Locate every leukocyte (white blood cell).
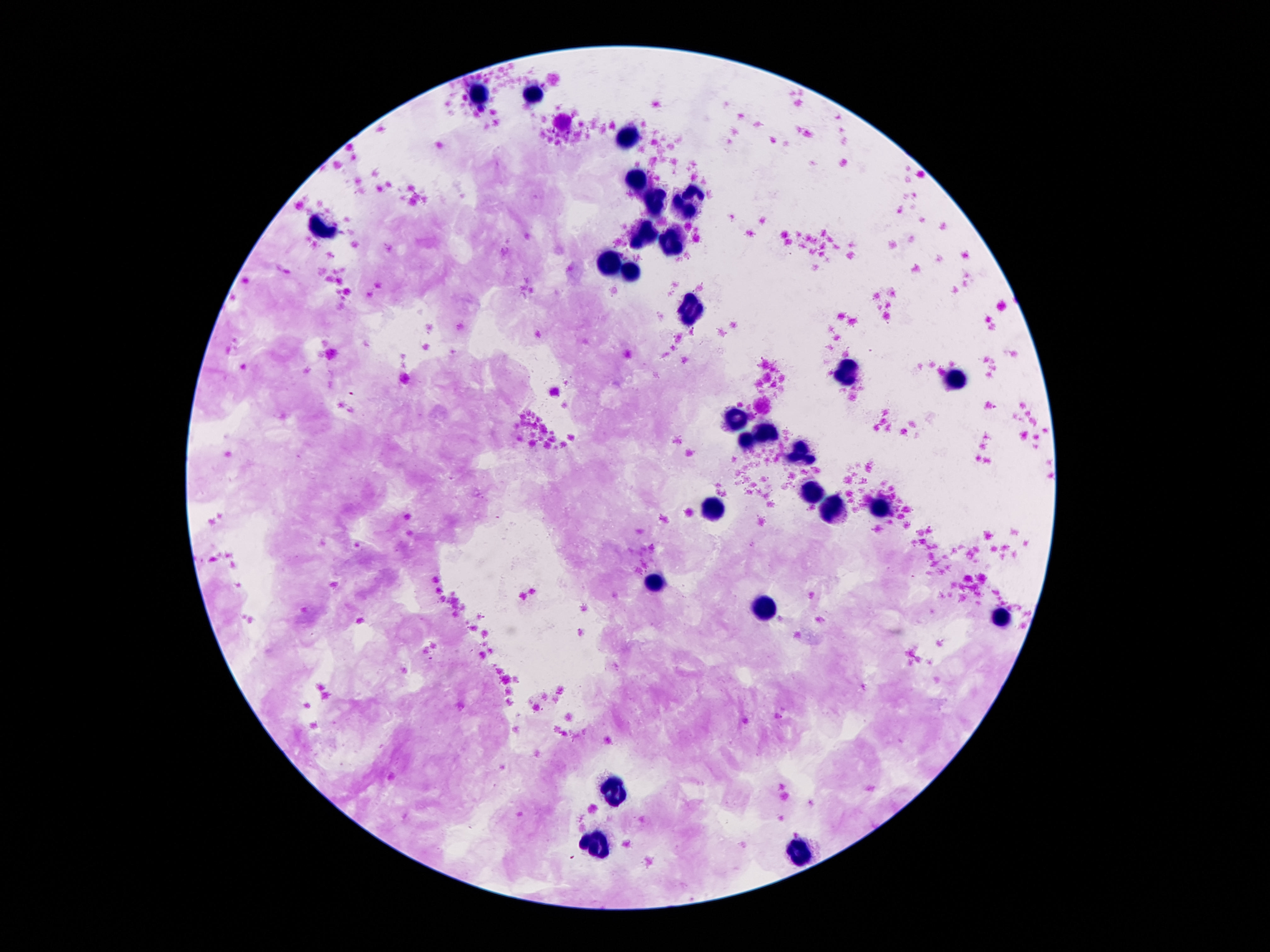

Approximate centers as (x, y) in pixels.
Leukocytes: (477, 93), (534, 94), (627, 137), (638, 183), (694, 198), (656, 201), (324, 228), (643, 240), (673, 245), (612, 262), (629, 272), (696, 305), (848, 370), (957, 380), (735, 420), (766, 435), (746, 442), (800, 455), (815, 495), (881, 506), (715, 510), (833, 513), (654, 585), (764, 608), (1001, 617), (614, 789), (598, 845), (802, 851).

Giemsa-stained preparation. Thick peripheral-blood smear. Single field of view. Patient malaria status: negative. Image is 1270×952 pixels. 100x magnification. Smartphone photograph taken through the microscope eyepiece.